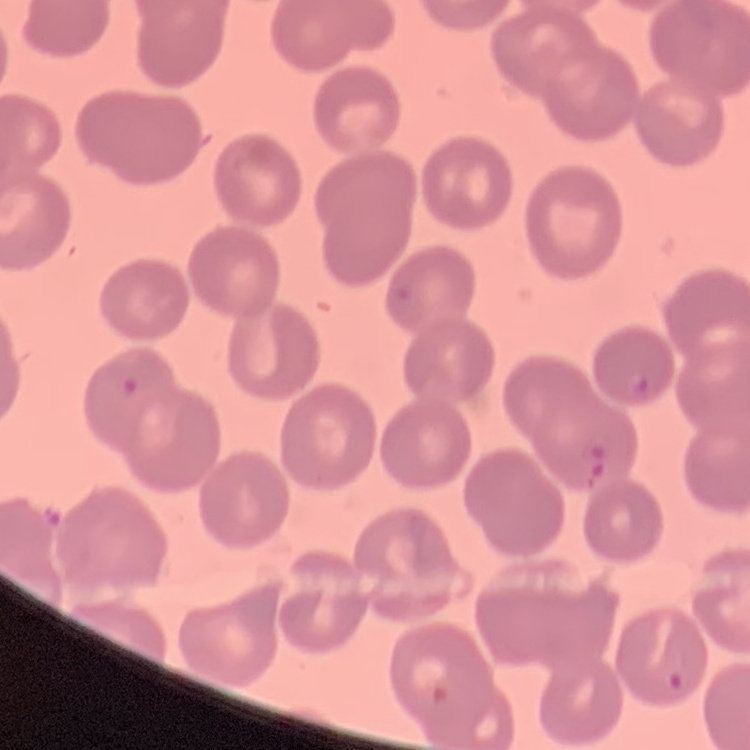

Summary:
  - Red blood cell morphology: no rouleaux formation
  - Image type: square crop of a larger photomicrograph
  - Preparation: thin peripheral smear
  - Stain: Field's or Giemsa